Assess this cell for malaria.
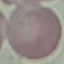

Uninfected.

Cell patch, automatically extracted from a larger field of view and resized to 64 × 64 pixels. Thin blood film. Giemsa stain. Acquired by smartphone through the microscope eyepiece.